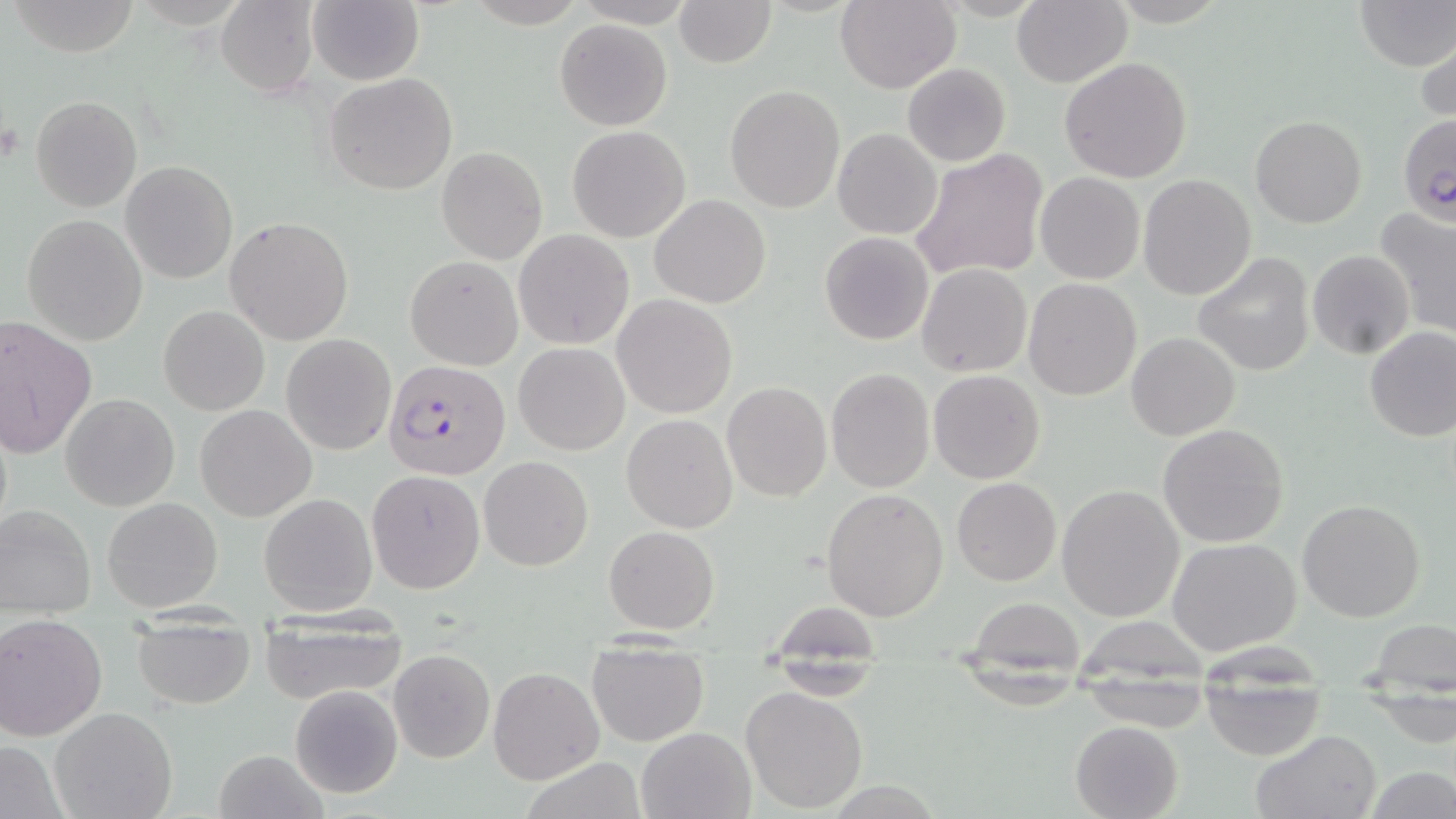
slide_level_diagnosis: Plasmodium falciparum
image_size: 1456×819 pixels
modality: light microscopy
field_of_view: one of a larger specimen
stain: May-Grünwald-Giemsa
magnification: 1000x
plasmodium_falciparum_infected_red_blood_cell_locations: 'approximate bounding boxes as named x1/y1/x2/y2 corners in pixels: (x1=1398, y1=113, x2=1456, y2=226), (x1=384, y1=360, x2=509, y2=480)'
preparation: thin blood film
uninfected_red_blood_cell_locations: 'approximate bounding boxes as named x1/y1/x2/y2 corners in pixels: (x1=215, y1=0, x2=319, y2=97), (x1=307, y1=0, x2=424, y2=86), (x1=673, y1=0, x2=776, y2=68), (x1=835, y1=0, x2=961, y2=93), (x1=1354, y1=0, x2=1455, y2=71), (x1=9, y1=1, x2=143, y2=57), (x1=1012, y1=1, x2=1131, y2=87), (x1=554, y1=19, x2=672, y2=131), (x1=1416, y1=35, x2=1456, y2=131), (x1=1060, y1=56, x2=1193, y2=185), (x1=902, y1=63, x2=1012, y2=166), (x1=322, y1=72, x2=458, y2=195), (x1=724, y1=84, x2=847, y2=213), (x1=31, y1=96, x2=141, y2=211), (x1=1250, y1=114, x2=1367, y2=228), (x1=567, y1=125, x2=690, y2=242), (x1=833, y1=129, x2=941, y2=239), (x1=436, y1=146, x2=548, y2=265), (x1=908, y1=149, x2=1049, y2=282), (x1=120, y1=161, x2=238, y2=284), (x1=1035, y1=172, x2=1145, y2=285), (x1=1138, y1=174, x2=1256, y2=300), (x1=650, y1=194, x2=770, y2=309), (x1=1375, y1=208, x2=1456, y2=340), (x1=21, y1=214, x2=148, y2=346), (x1=223, y1=217, x2=355, y2=345), (x1=513, y1=229, x2=634, y2=349), (x1=820, y1=231, x2=934, y2=345), (x1=1307, y1=250, x2=1415, y2=359), (x1=1194, y1=252, x2=1315, y2=375), (x1=405, y1=255, x2=522, y2=369), (x1=917, y1=264, x2=1032, y2=378), (x1=1024, y1=278, x2=1143, y2=401), (x1=612, y1=294, x2=738, y2=419), (x1=158, y1=304, x2=269, y2=416), (x1=0, y1=315, x2=97, y2=459), (x1=1364, y1=325, x2=1456, y2=442), (x1=1126, y1=332, x2=1240, y2=441), (x1=281, y1=334, x2=396, y2=456), (x1=514, y1=342, x2=630, y2=455), (x1=826, y1=368, x2=934, y2=494), (x1=928, y1=369, x2=1045, y2=484), (x1=722, y1=382, x2=831, y2=501), (x1=61, y1=394, x2=179, y2=511), (x1=195, y1=404, x2=317, y2=522), (x1=621, y1=413, x2=738, y2=533), (x1=1158, y1=422, x2=1290, y2=549), (x1=479, y1=455, x2=593, y2=570), (x1=366, y1=470, x2=484, y2=593), (x1=952, y1=477, x2=1061, y2=585), (x1=1057, y1=483, x2=1185, y2=621), (x1=821, y1=487, x2=949, y2=621), (x1=259, y1=492, x2=379, y2=615), (x1=102, y1=497, x2=222, y2=612), (x1=1297, y1=497, x2=1425, y2=622), (x1=0, y1=504, x2=97, y2=617), (x1=603, y1=525, x2=720, y2=635), (x1=1168, y1=536, x2=1303, y2=656), (x1=967, y1=598, x2=1087, y2=664), (x1=259, y1=611, x2=409, y2=703), (x1=0, y1=612, x2=110, y2=742), (x1=131, y1=617, x2=256, y2=709), (x1=1368, y1=618, x2=1454, y2=690), (x1=586, y1=644, x2=710, y2=746), (x1=389, y1=648, x2=496, y2=763), (x1=766, y1=663, x2=884, y2=700), (x1=488, y1=666, x2=604, y2=785), (x1=289, y1=684, x2=402, y2=799), (x1=1200, y1=685, x2=1324, y2=762), (x1=740, y1=686, x2=869, y2=814), (x1=1368, y1=692, x2=1455, y2=746), (x1=51, y1=707, x2=178, y2=819), (x1=1069, y1=720, x2=1184, y2=819), (x1=635, y1=726, x2=757, y2=819), (x1=1250, y1=729, x2=1382, y2=819), (x1=0, y1=740, x2=68, y2=818), (x1=213, y1=749, x2=329, y2=819), (x1=519, y1=756, x2=649, y2=819), (x1=1365, y1=766, x2=1453, y2=819)'